Report the malaria status of this cell.
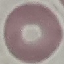

It is uninfected.

Giemsa-stained preparation. Photographed with a smartphone camera at the microscope eyepiece. Automatically extracted cell patch, resized to 64 × 64 pixels. Thin blood film.